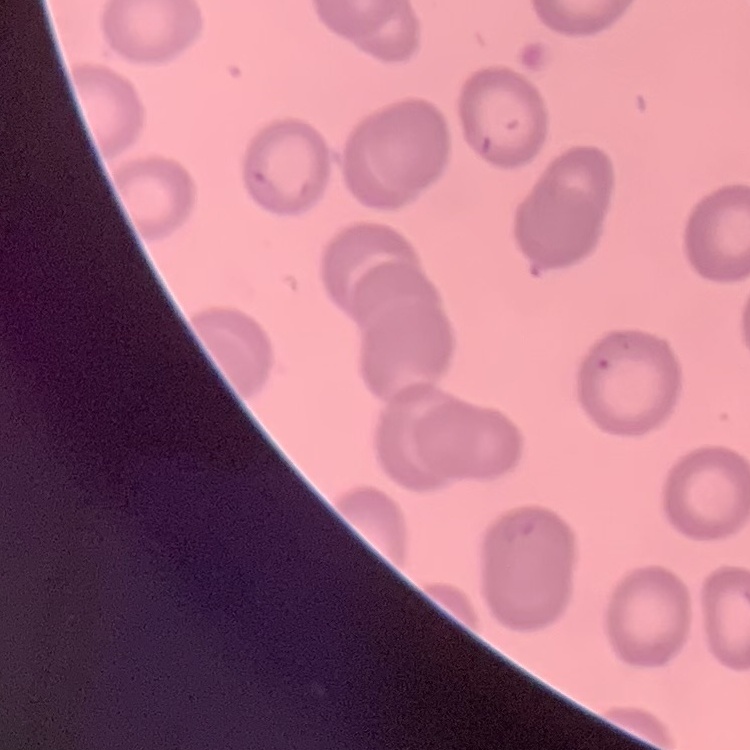

The erythrocytes exhibit no rouleaux formation. One tile cut from a larger photomicrograph. Field's or Giemsa stain. Thin blood smear.